Assess this cell for malaria.
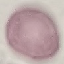

It is uninfected.

Summary:
  - Capture: smartphone camera at the microscope eyepiece
  - Preparation: thin smear
  - Image type: automatically extracted cell patch, resized to 64 × 64 pixels
  - Stain: Giemsa